Assess this cell for malaria.
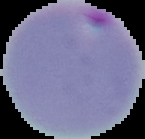
It is parasitized.

Image is 145×139 pixels. The area outside the segmented cell region is set to black. From a thin blood smear.